Name the parasite shown.
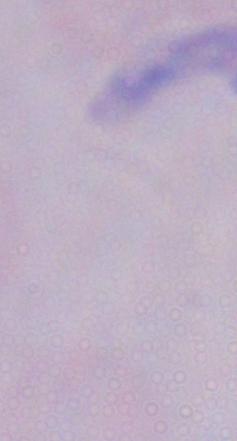

A trypanosome.

1000x magnification. Micrograph.